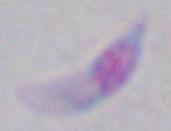
Summary:
  - Magnification: 1000x
  - Identification: Toxoplasma gondii
  - Modality: photomicrograph